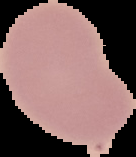
The area outside the segmented cell region is set to black. Malaria status: uninfected. Image is 136×157 pixels. From a thin blood smear.